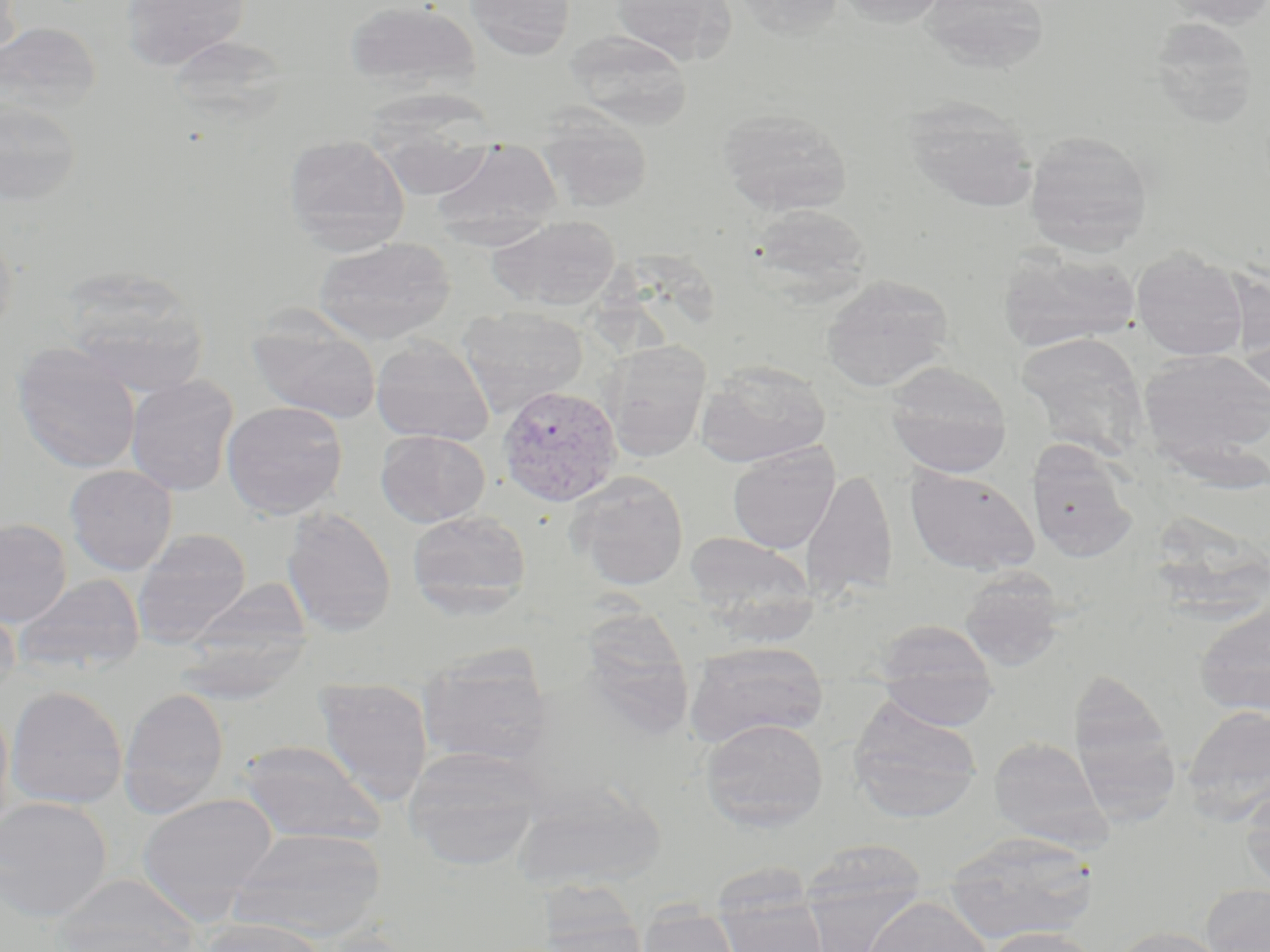
slide-level diagnosis = Plasmodium vivax
stain = May-Grünwald-Giemsa
Plasmodium vivax-infected red blood cell locations = approximate bounding boxes as [x1, y1, x2, y2] in pixels: [497, 384, 622, 507]
preparation = thin blood smear
modality = optical microscopy
uninfected red blood cell locations = approximate bounding boxes as [x1, y1, x2, y2] in pixels: [0, 0, 24, 64], [119, 0, 250, 70], [344, 0, 480, 94], [465, 0, 576, 60], [612, 0, 736, 64], [732, 0, 846, 39], [836, 0, 950, 28], [918, 0, 1051, 74], [1160, 0, 1270, 29], [1146, 16, 1261, 127], [0, 21, 103, 123], [564, 30, 693, 129], [166, 35, 290, 126], [0, 96, 84, 206], [903, 96, 1039, 213], [717, 107, 853, 216], [538, 110, 653, 212], [370, 123, 498, 201], [1024, 130, 1154, 254], [282, 132, 411, 253], [432, 140, 564, 237], [747, 203, 873, 302], [488, 216, 620, 310], [0, 219, 18, 343], [314, 237, 456, 344], [996, 246, 1141, 354], [1131, 247, 1248, 361], [58, 265, 208, 395], [820, 274, 953, 392], [1230, 279, 1270, 390], [458, 307, 588, 416], [247, 313, 382, 424], [1016, 333, 1148, 458], [371, 337, 494, 445], [602, 341, 711, 461], [11, 342, 141, 474], [1137, 350, 1270, 470], [695, 360, 830, 466], [884, 361, 1012, 477], [125, 375, 238, 496], [221, 401, 348, 519], [384, 426, 519, 612], [375, 429, 490, 527], [728, 444, 840, 553], [1027, 444, 1139, 563], [65, 465, 178, 575], [904, 465, 1040, 576], [801, 468, 898, 603], [566, 471, 689, 590], [281, 506, 397, 636], [407, 510, 531, 618], [0, 518, 72, 628], [131, 529, 252, 648], [683, 531, 817, 637], [959, 569, 1066, 671], [13, 573, 145, 678], [183, 578, 313, 672], [590, 600, 693, 739], [1194, 601, 1270, 716], [0, 602, 20, 704], [876, 621, 998, 725], [172, 632, 311, 704], [684, 642, 829, 746], [418, 652, 553, 768], [1067, 669, 1180, 814], [314, 677, 433, 804], [5, 686, 128, 810], [118, 687, 229, 816], [847, 697, 982, 822], [0, 701, 14, 840], [1182, 704, 1270, 821], [700, 718, 829, 831], [988, 737, 1107, 847], [236, 740, 386, 846], [403, 745, 544, 869], [512, 780, 666, 893], [1241, 785, 1270, 893], [136, 792, 278, 921], [0, 796, 112, 922], [228, 828, 386, 940], [943, 831, 1098, 945], [801, 838, 927, 948], [52, 876, 203, 952], [1201, 883, 1270, 952], [716, 888, 829, 952], [530, 894, 650, 952], [862, 897, 992, 952], [637, 907, 743, 952], [197, 917, 328, 952], [1108, 925, 1231, 952], [984, 926, 1101, 952]
magnification = 1000x
field of view = one of a larger specimen
image size = 1270×952 pixels